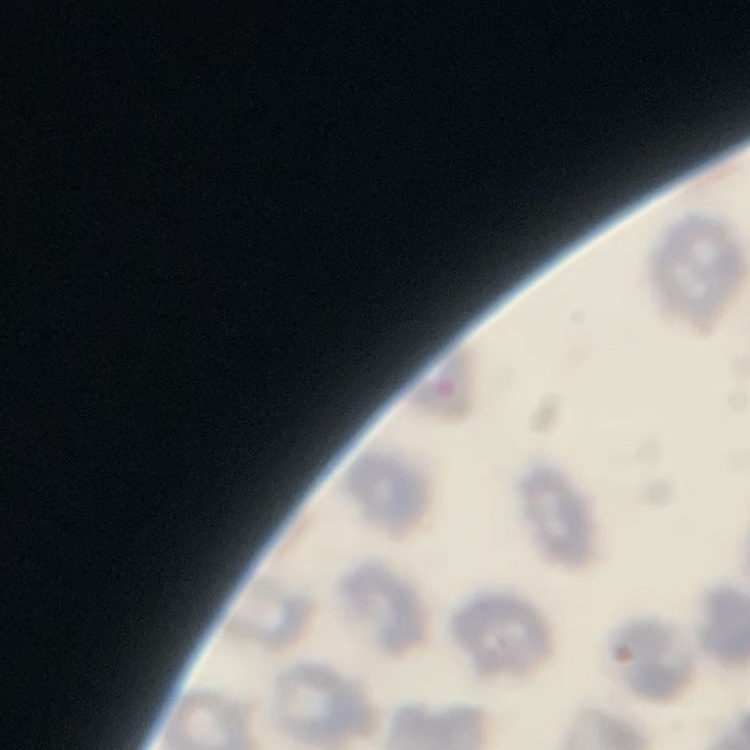
{
  "erythrocyte_morphology": "no rouleaux formation",
  "image_type": "square crop of a larger photomicrograph",
  "preparation": "thin blood film",
  "stain": "Field's or Giemsa"
}